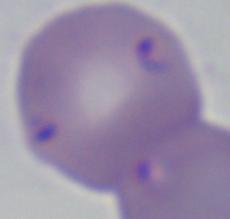
Captured at 1000x magnification. A Babesia parasite is seen. Photomicrograph.